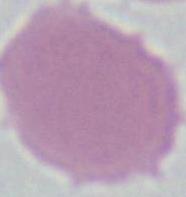
Summary:
  - Magnification: 1000x
  - Identification: red blood cell
  - Modality: micrograph